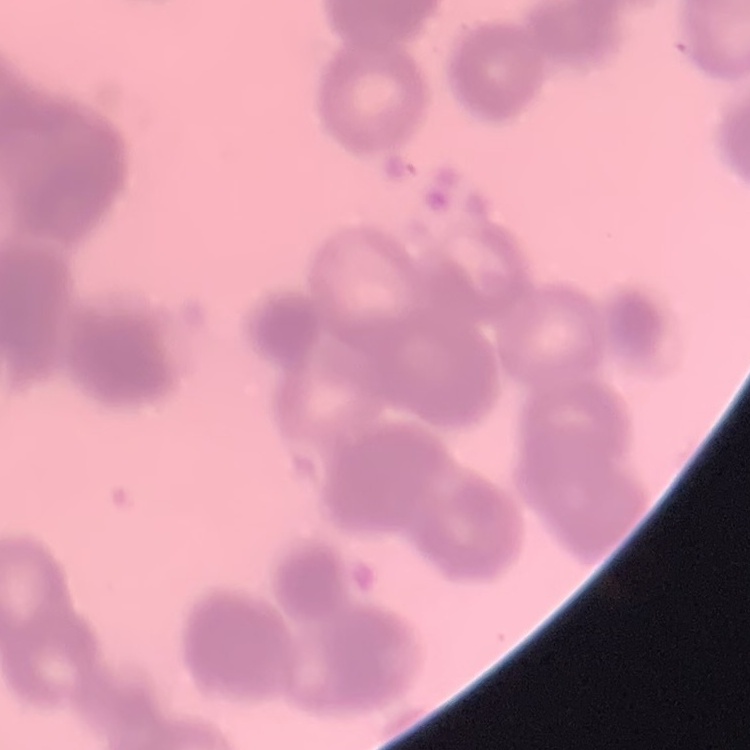 The erythrocytes exhibit rouleaux formation. One tile cut from a larger photomicrograph. Thin blood smear. Field's or Giemsa stain.